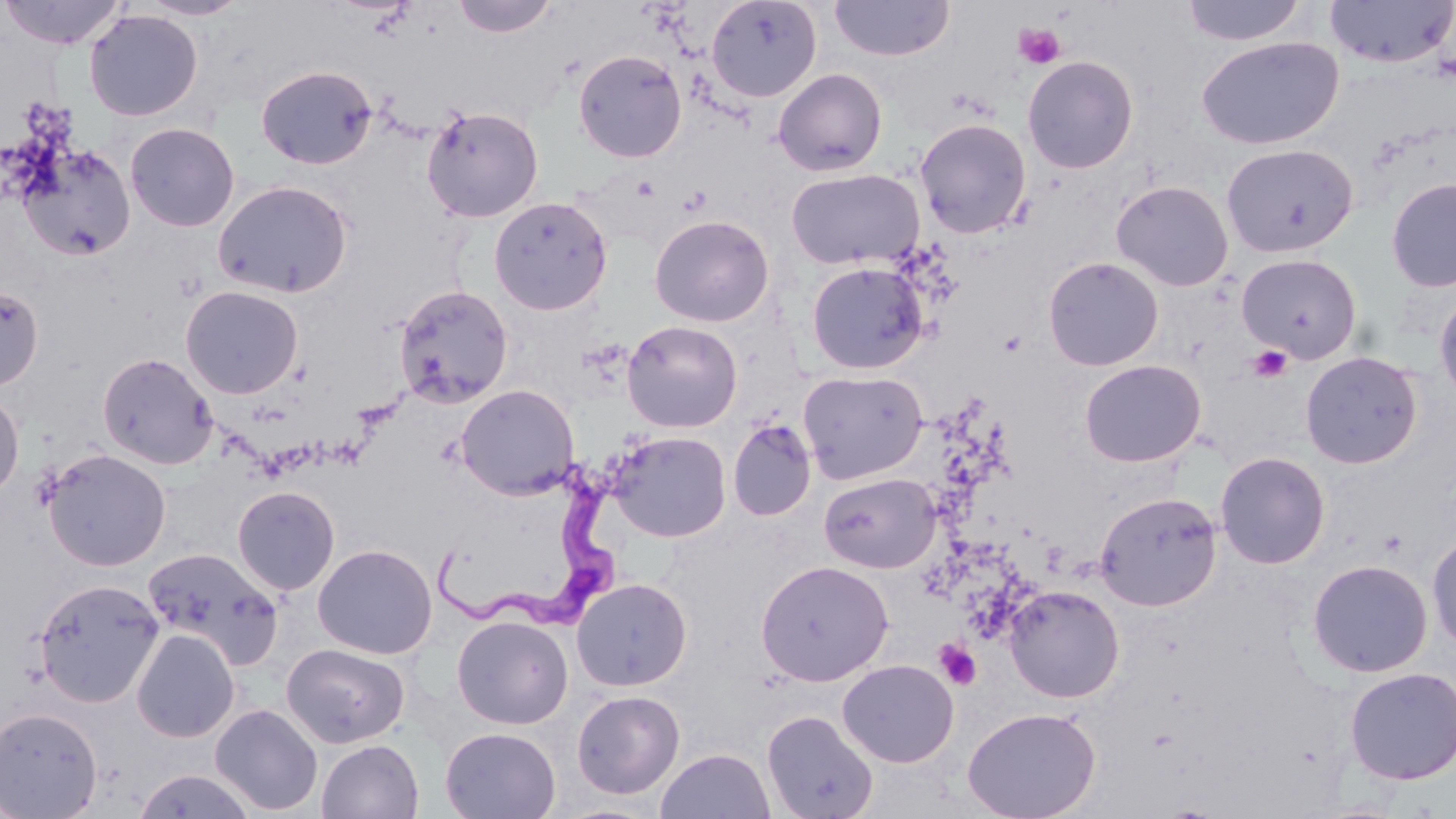

Summary:
  - Coordinate format: approximate bounding boxes as [x1, y1, x2, y2] in pixels
  - Trypanosoma brucei locations: [430, 470, 629, 636]
  - Uninfected red blood cell locations: [136, 0, 252, 20], [452, 0, 558, 38], [706, 0, 822, 102], [830, 0, 954, 61], [1324, 0, 1456, 68], [0, 1, 127, 49], [1180, 1, 1308, 46], [84, 9, 203, 121], [1195, 36, 1345, 150], [573, 49, 687, 163], [1022, 55, 1139, 174], [256, 65, 377, 169], [773, 68, 887, 176], [421, 104, 544, 222], [914, 117, 1032, 238], [124, 122, 239, 232], [17, 143, 136, 261], [1220, 143, 1358, 258], [785, 167, 924, 271], [1385, 177, 1456, 293], [212, 179, 353, 298], [1111, 180, 1234, 291], [489, 196, 613, 315], [649, 214, 775, 327], [1236, 253, 1362, 362], [1043, 256, 1164, 371], [806, 261, 929, 374], [0, 284, 43, 391], [393, 284, 514, 408], [180, 285, 303, 399], [1433, 288, 1456, 408], [621, 320, 743, 432], [1300, 351, 1422, 469], [97, 352, 219, 470], [1079, 359, 1205, 467], [798, 370, 928, 484], [455, 384, 579, 500], [0, 387, 25, 501], [728, 419, 816, 521], [607, 430, 731, 542], [42, 449, 171, 571], [1215, 451, 1331, 569], [818, 472, 939, 574], [231, 485, 340, 595], [1094, 491, 1222, 611], [1426, 531, 1456, 654], [313, 543, 438, 659], [143, 546, 284, 670], [755, 559, 894, 686], [1307, 559, 1433, 678], [33, 577, 164, 707], [571, 577, 692, 690], [1004, 584, 1124, 703], [451, 615, 574, 729], [131, 628, 240, 743], [281, 643, 409, 748], [838, 659, 959, 767], [1343, 666, 1456, 784], [571, 690, 685, 799], [209, 703, 323, 815], [0, 706, 103, 818], [962, 706, 1101, 819], [761, 709, 880, 819], [440, 727, 561, 818], [316, 739, 423, 819], [655, 748, 775, 819], [132, 769, 257, 819]
  - Platelet locations: [1012, 22, 1067, 70], [1247, 345, 1293, 383], [934, 638, 981, 690]
  - Slide-level diagnosis: Trypanosoma brucei
  - Stain: May-Grünwald-Giemsa
  - Preparation: thin blood film
  - Modality: optical microscopy
  - Magnification: 1000x
  - Image size: 1456×819 pixels
  - Field of view: single